Report the malaria status of this cell.
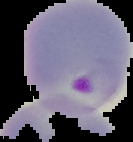
Parasitized.

Summary:
  - Image size: 133×142 pixels
  - Preparation: thin blood film
  - Image type: cell region segmented out of the field of view; surrounding area masked to black